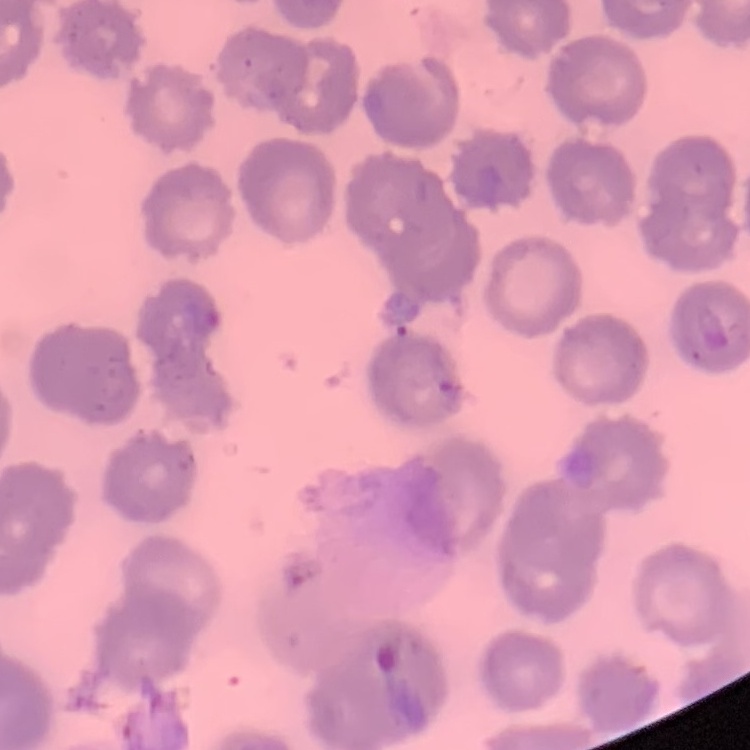
The red blood cells show no rouleaux formation. Square crop of a larger photomicrograph. Stained with either Field's or Giemsa. Thin blood smear.